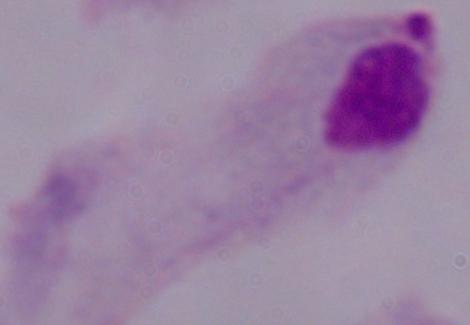
Summary:
  - Identification: trichomonad
  - Magnification: 1000x
  - Modality: photomicrograph